Assess the morphology of the red blood cells.
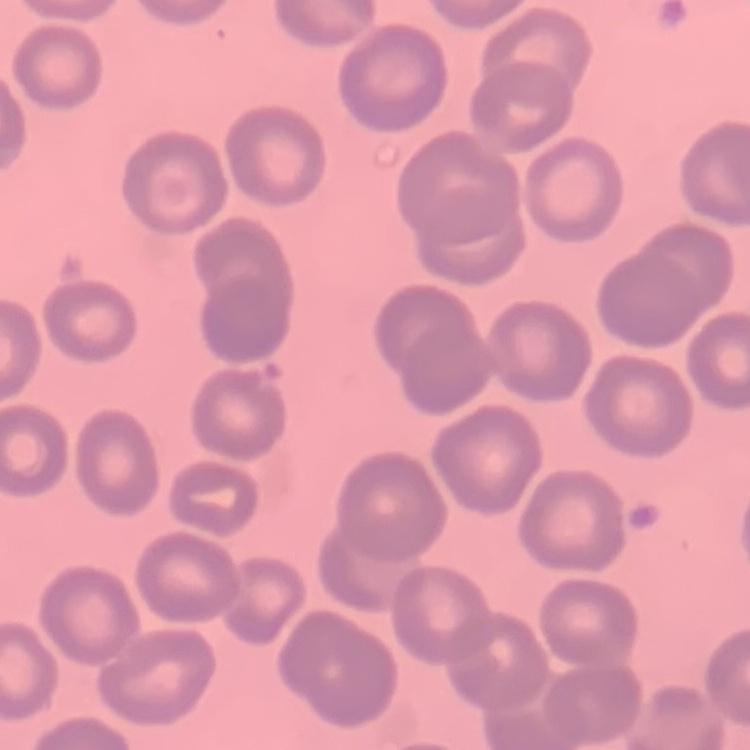

They show no rouleaux formation.

preparation: thin blood film
image_type: square crop of a larger photomicrograph
stain: Field's or Giemsa